Name the blood parasite species.
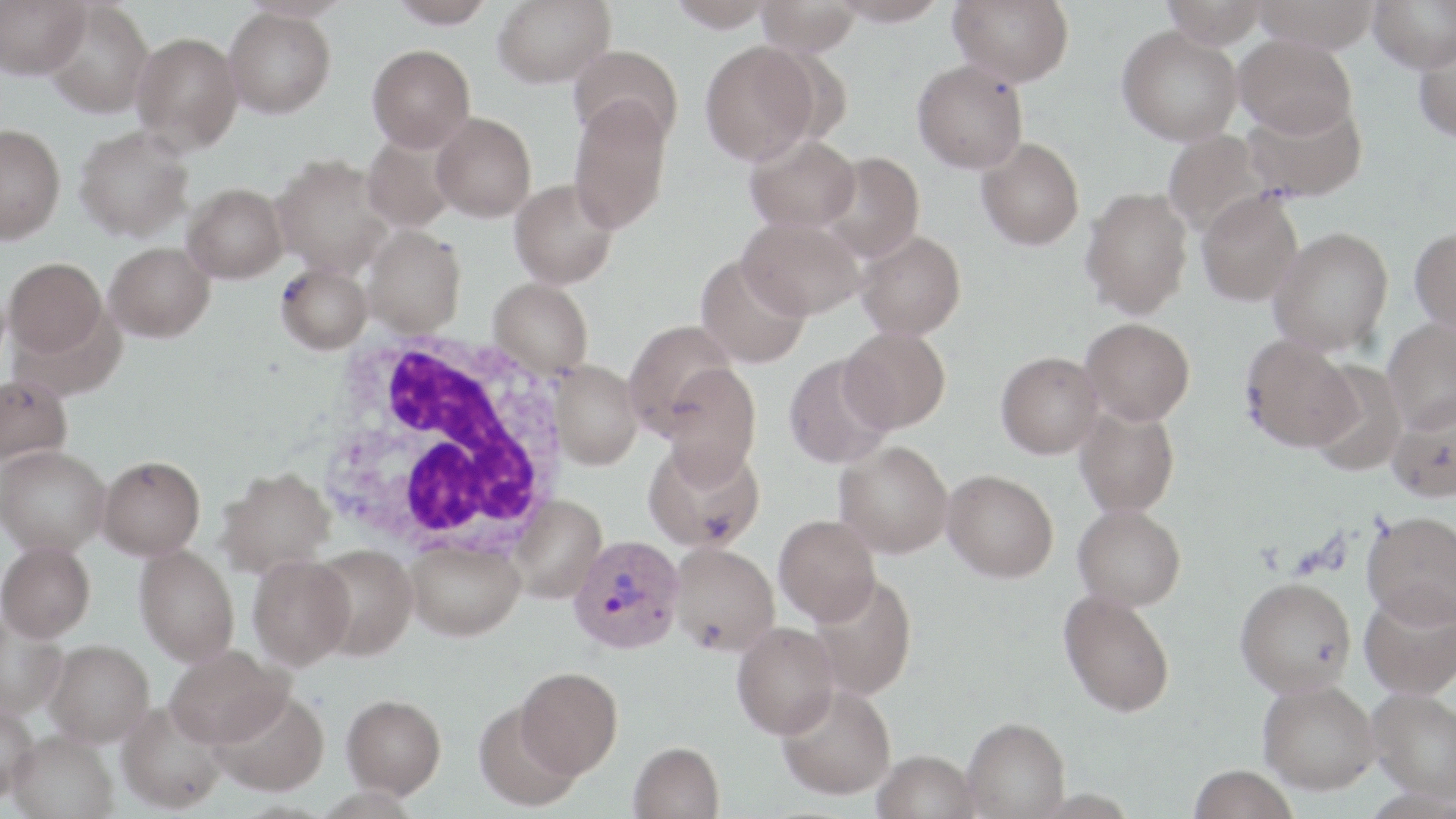

Plasmodium vivax.

Approximate bounding boxes as (x1, y1, x2, y2) in pixels. Plasmodium vivax-infected red blood cell locations: (569, 535, 683, 654). White blood cell locations: (311, 328, 572, 564). Uninfected red blood cell locations: (0, 0, 89, 78), (389, 0, 495, 28), (493, 0, 615, 88), (667, 0, 777, 31), (829, 0, 948, 26), (948, 0, 1074, 86), (1162, 0, 1269, 48), (1252, 0, 1381, 52), (1368, 0, 1456, 72), (43, 1, 155, 118), (756, 1, 861, 56), (224, 7, 336, 118), (1117, 25, 1242, 146), (132, 32, 243, 153), (1234, 33, 1357, 138), (1413, 36, 1456, 143), (700, 41, 819, 165), (367, 45, 475, 153), (568, 45, 683, 146), (912, 59, 1028, 174), (568, 98, 673, 233), (1243, 99, 1367, 203), (431, 112, 537, 221), (0, 124, 65, 244), (74, 125, 194, 242), (1162, 130, 1276, 237), (361, 133, 459, 232), (745, 133, 861, 233), (976, 138, 1085, 250), (818, 152, 925, 262), (271, 154, 395, 277), (509, 178, 619, 289), (183, 183, 288, 283), (1080, 186, 1193, 318), (1196, 190, 1303, 306), (737, 216, 866, 320), (363, 226, 466, 336), (1269, 226, 1393, 356), (1410, 226, 1456, 332), (855, 229, 966, 340), (105, 242, 214, 342), (695, 253, 811, 369), (4, 257, 107, 357), (275, 263, 372, 353), (488, 277, 594, 378), (1080, 317, 1194, 425), (624, 319, 738, 435), (1382, 319, 1456, 433), (839, 327, 951, 432), (1240, 334, 1360, 452), (995, 351, 1104, 458), (783, 353, 895, 470), (551, 360, 644, 470), (660, 362, 762, 481), (1307, 362, 1407, 476), (0, 374, 73, 466), (1386, 400, 1456, 504), (1073, 403, 1181, 518), (643, 439, 765, 552), (834, 440, 953, 558), (1, 445, 110, 556), (97, 455, 205, 559), (216, 467, 335, 576), (942, 469, 1058, 582), (509, 495, 606, 603), (1073, 503, 1186, 611), (1362, 510, 1456, 629), (774, 514, 880, 624), (0, 541, 96, 642), (405, 541, 525, 640), (669, 542, 780, 655), (309, 544, 418, 660), (134, 545, 240, 666), (248, 554, 355, 670), (807, 572, 918, 701), (1235, 577, 1357, 697), (1058, 589, 1176, 717), (1360, 589, 1456, 700), (0, 611, 68, 719), (732, 621, 839, 739), (46, 639, 154, 746), (166, 644, 291, 747), (516, 667, 623, 778), (1257, 678, 1379, 794), (777, 683, 896, 800), (210, 687, 329, 796), (1367, 687, 1456, 804), (341, 693, 446, 797), (0, 701, 39, 800), (117, 701, 228, 813), (473, 701, 582, 811), (963, 717, 1070, 818), (7, 730, 119, 819), (629, 741, 724, 819), (872, 750, 981, 819), (1187, 765, 1299, 819). Single field of view. Image is 1456×819 pixels. May-Grünwald-Giemsa stain. Light microscopy. Thin blood smear. Captured at 1000x magnification.